Locate every uninfected red blood cell.
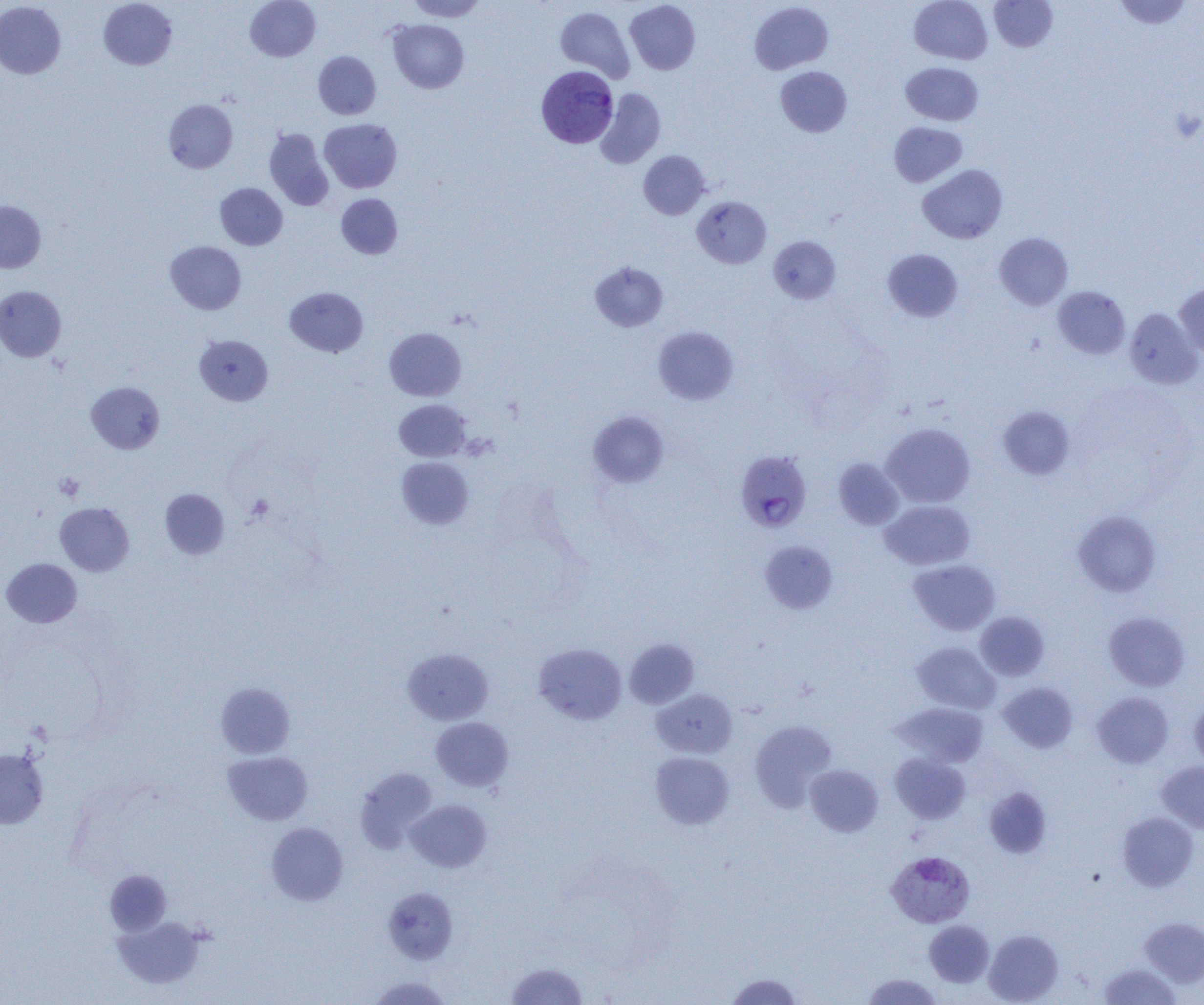
Approximate bounding boxes as (x1, y1, x2, y2) in pixels.
Uninfected red blood cells: (98, 0, 177, 70), (245, 0, 320, 61), (407, 0, 489, 21), (909, 0, 992, 64), (1111, 0, 1194, 29), (0, 1, 66, 79), (625, 1, 701, 75), (749, 1, 833, 74), (989, 1, 1058, 52), (555, 6, 635, 82), (388, 19, 469, 93), (313, 51, 381, 119), (900, 62, 984, 126), (776, 66, 852, 137), (595, 88, 666, 169), (163, 99, 238, 173), (319, 119, 402, 193), (889, 122, 967, 187), (264, 128, 334, 211), (638, 151, 710, 219), (917, 164, 1008, 244), (215, 183, 287, 250), (336, 193, 403, 259), (691, 196, 771, 268), (0, 200, 46, 272), (994, 232, 1073, 310), (768, 236, 841, 304), (165, 241, 246, 315), (883, 248, 963, 322), (590, 261, 668, 332), (1174, 283, 1204, 358), (0, 286, 66, 361), (1052, 286, 1130, 359), (285, 287, 368, 357), (1124, 308, 1203, 389), (653, 325, 739, 405), (384, 327, 466, 400), (194, 334, 273, 405), (86, 381, 165, 454), (394, 399, 471, 461), (997, 405, 1076, 479), (588, 411, 669, 487), (881, 423, 975, 508), (396, 456, 473, 529), (833, 458, 904, 530), (160, 488, 229, 559), (880, 500, 975, 570), (55, 502, 134, 576), (1073, 511, 1161, 597), (759, 540, 838, 614), (1, 558, 82, 627), (908, 559, 1000, 635), (1103, 611, 1190, 691), (975, 612, 1049, 681), (624, 639, 699, 709), (912, 642, 1000, 714), (534, 643, 627, 725), (402, 648, 493, 725), (215, 682, 296, 758), (998, 682, 1078, 752), (651, 689, 738, 759), (1092, 692, 1174, 768), (1189, 699, 1204, 772), (894, 702, 989, 767), (431, 717, 514, 791), (749, 720, 837, 811), (0, 749, 48, 828), (222, 751, 313, 825), (650, 752, 734, 829), (890, 752, 970, 823), (1157, 761, 1204, 834), (805, 765, 883, 837), (355, 767, 438, 852), (985, 787, 1052, 859), (407, 799, 492, 872), (1117, 812, 1198, 891), (266, 822, 349, 905), (105, 869, 171, 935), (382, 887, 458, 964), (111, 915, 207, 989), (1140, 918, 1204, 987), (924, 920, 994, 987), (984, 929, 1063, 1004), (506, 961, 589, 1004), (1097, 963, 1181, 1004), (725, 972, 804, 1004), (860, 973, 944, 1004), (368, 975, 453, 1004).

Summary:
  - Plasmodium vivax-infected red blood cell locations: (537, 67, 622, 149), (735, 450, 811, 532), (886, 851, 975, 928)
  - Platelet locations: (1170, 106, 1203, 144), (54, 473, 84, 500), (247, 495, 273, 520)
  - Slide-level diagnosis: Plasmodium vivax
  - Image size: 1204×1005 pixels
  - Field of view: single
  - Modality: light microscopy
  - Magnification: 1000x
  - Preparation: thin blood film